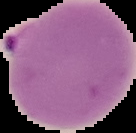
Cell region segmented out of the field of view; the surrounding area is masked to black. Result: Plasmodium parasites detected. From a thin blood smear. Image is 136×133 pixels.